Report the malaria status of this cell.
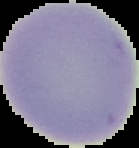

It is uninfected.

From a thin blood film. The area outside the segmented cell region is set to black. Image is 139×148 pixels.